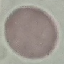 Malaria status: uninfected. Giemsa-stained preparation. Thin blood smear. Automatically extracted cell patch, resized to 64 × 64 pixels. Photographed with a smartphone camera at the microscope eyepiece.